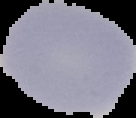
Malaria status: uninfected. From a thin blood smear. Image is 136×118 pixels. The area outside the segmented cell region is set to black.